Locate and identify every blood parasite.
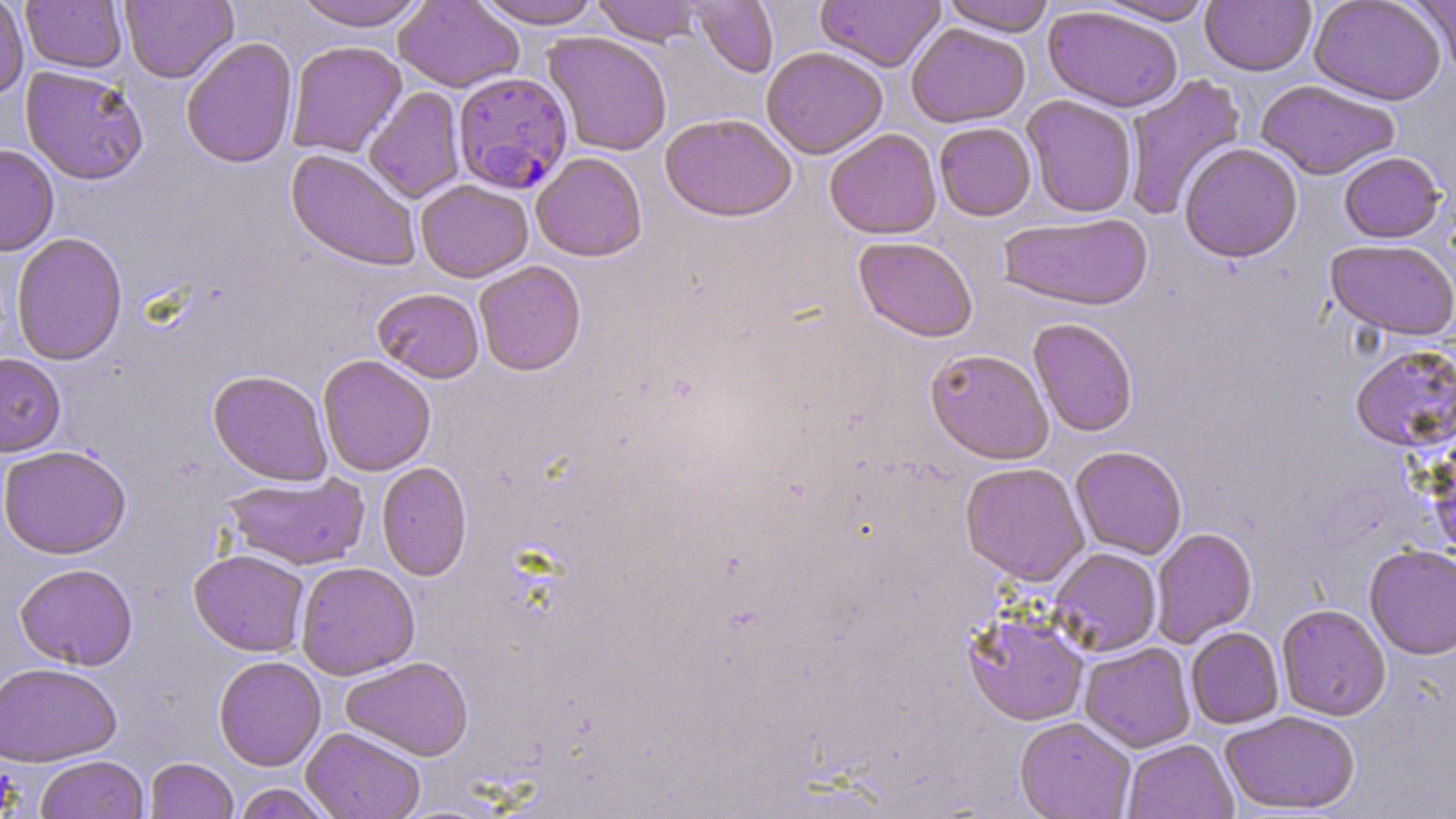
Approximate bounding boxes as (x1, y1, x2, y2) in pixels.
Plasmodium falciparum-infected red blood cells: (453, 71, 573, 195).
No Plasmodium ovale, Plasmodium malariae, Plasmodium vivax, Babesia divergens, or Trypanosoma brucei observed.

{
  "slide_level_diagnosis": "Plasmodium falciparum",
  "image_size": "1456×819 pixels",
  "uninfected_red_blood_cell_locations": "approximate bounding boxes as (x1, y1, x2, y2) in pixels: (0, 0, 29, 100), (120, 0, 238, 84), (291, 0, 430, 31), (394, 0, 523, 93), (475, 0, 602, 29), (592, 0, 702, 46), (687, 0, 779, 78), (940, 0, 1057, 36), (1095, 0, 1215, 25), (1309, 0, 1446, 106), (1408, 0, 1455, 77), (21, 1, 127, 74), (815, 1, 945, 72), (1200, 1, 1316, 76), (1043, 6, 1182, 113), (906, 23, 1030, 128), (542, 31, 673, 157), (181, 37, 299, 169), (286, 40, 408, 158), (761, 46, 888, 159), (20, 65, 149, 185), (1121, 74, 1247, 221), (1256, 80, 1400, 181), (363, 87, 466, 203), (1022, 95, 1138, 218), (660, 113, 797, 223), (934, 122, 1036, 222), (824, 128, 941, 239), (0, 143, 59, 256), (1179, 143, 1303, 263), (286, 149, 422, 271), (531, 152, 647, 261), (1339, 152, 1446, 243), (415, 179, 534, 283), (996, 213, 1153, 311), (10, 232, 128, 366), (853, 236, 978, 342), (1325, 239, 1456, 341), (474, 260, 586, 376), (372, 287, 485, 383), (1028, 318, 1138, 438), (1350, 343, 1456, 454), (925, 349, 1053, 465), (0, 353, 66, 457), (317, 355, 436, 477), (207, 370, 333, 486), (1425, 433, 1456, 560), (0, 445, 131, 558), (1069, 446, 1188, 559), (376, 461, 472, 581), (959, 462, 1090, 586), (223, 472, 369, 571), (1150, 527, 1257, 648), (1364, 544, 1456, 660), (1049, 548, 1161, 657), (189, 549, 310, 656), (295, 561, 420, 680), (14, 563, 138, 670), (1276, 603, 1391, 721), (962, 609, 1089, 726), (1185, 627, 1284, 729), (1079, 642, 1196, 752), (213, 655, 326, 771), (340, 656, 473, 761), (0, 662, 122, 766), (1220, 710, 1360, 815), (1015, 718, 1136, 819), (301, 727, 426, 819), (1122, 739, 1237, 819), (35, 755, 149, 819), (145, 758, 238, 819), (231, 783, 338, 819)",
  "modality": "optical microscopy",
  "field_of_view": "single",
  "magnification": "1000x",
  "stain": "May-Grünwald-Giemsa",
  "preparation": "thin blood film"
}